State which cell type is depicted.
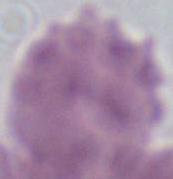
An erythrocyte.

Summary:
  - Magnification: 1000x
  - Modality: micrograph